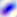
modality = photomicrograph
identification = Toxoplasma gondii
magnification = 400x